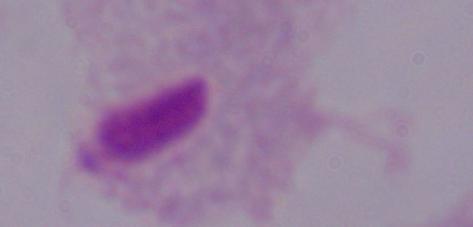
1000x magnification. A trichomonad is shown. Micrograph.